State which parasite is depicted.
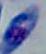
This is Toxoplasma gondii.

{
  "magnification": "1000x",
  "modality": "photomicrograph"
}